Locate every blood parasite and identify its species.
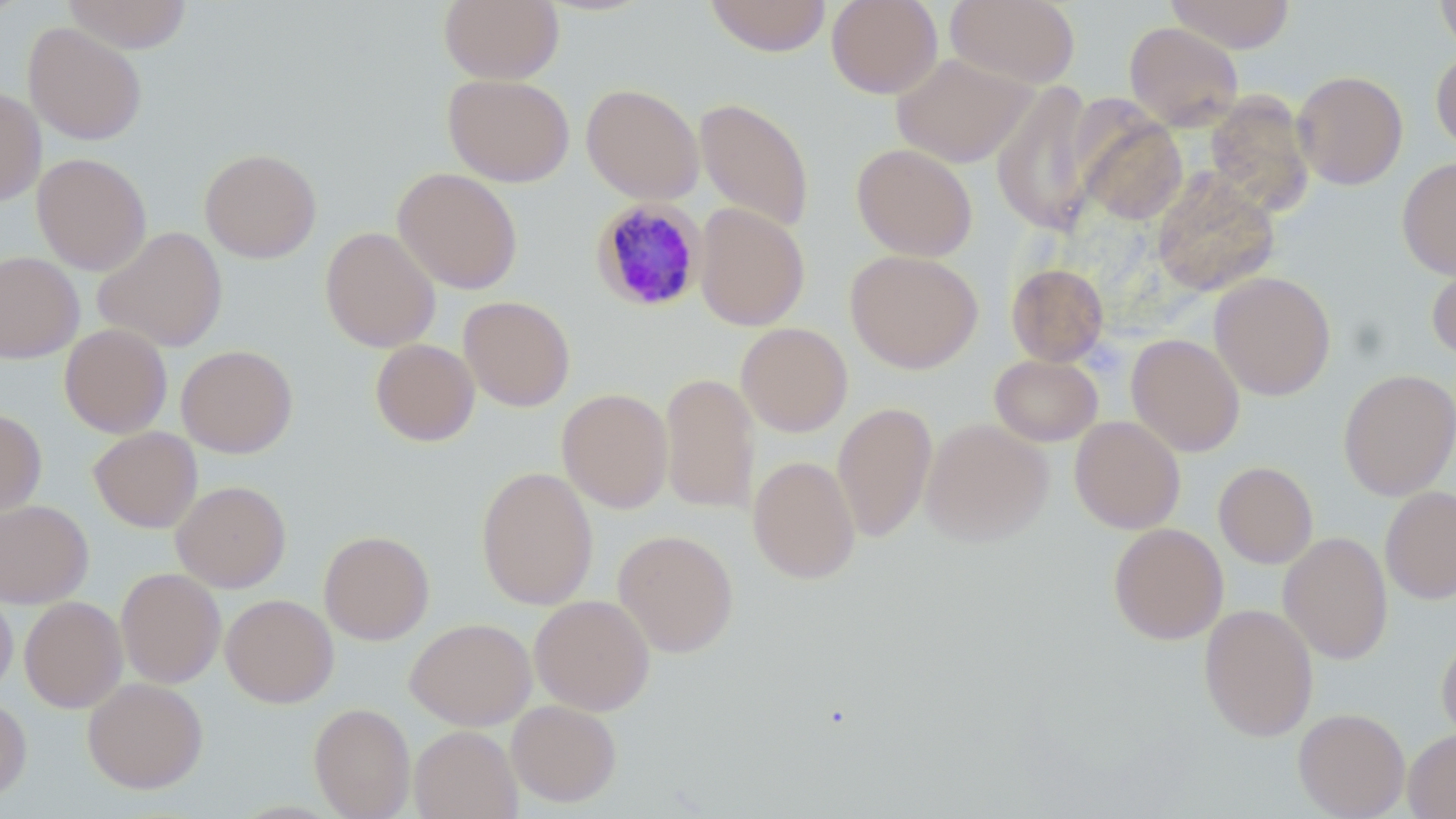
Approximate bounding boxes as (x1,y1)-(x2,y2) corner pairs in pixels.
Plasmodium malariae-infected red blood cells: (590,197)-(709,312).
No Plasmodium falciparum, Plasmodium ovale, Plasmodium vivax, Babesia divergens, or Trypanosoma brucei observed.

{
  "slide_level_diagnosis": "Plasmodium malariae",
  "uninfected_red_blood_cell_locations": "approximate bounding boxes as (x1,y1)-(x2,y2) corner pairs in pixels: (62,0)-(193,53), (438,0)-(564,84), (704,0)-(832,57), (826,0)-(943,98), (945,0)-(1081,89), (1164,0)-(1296,53), (1435,0)-(1456,56), (23,22)-(147,145), (1124,22)-(1243,131), (1431,49)-(1456,155), (891,52)-(1036,168), (1292,69)-(1408,189), (443,73)-(575,187), (991,82)-(1098,236), (581,83)-(704,204), (0,86)-(46,206), (1204,90)-(1315,217), (694,97)-(815,234), (1078,112)-(1187,226), (851,143)-(978,261), (199,147)-(321,263), (31,152)-(151,275), (1397,157)-(1456,280), (392,167)-(523,294), (1151,172)-(1280,296), (694,203)-(810,331), (320,226)-(440,352), (93,227)-(228,352), (845,249)-(983,373), (0,251)-(84,363), (1426,254)-(1456,361), (1006,262)-(1109,366), (1209,271)-(1336,400), (459,296)-(575,412), (736,322)-(852,437), (59,323)-(172,438), (1126,333)-(1245,457), (59,337)-(294,444), (370,339)-(480,446), (176,344)-(298,458), (989,354)-(1103,447), (1338,369)-(1456,500), (659,373)-(758,513), (556,388)-(673,513), (832,401)-(937,542), (0,408)-(47,517), (1069,415)-(1186,533), (920,417)-(1053,547), (88,426)-(202,532), (748,455)-(861,584), (1214,461)-(1318,568), (476,466)-(599,610), (171,480)-(291,592), (1380,485)-(1456,605), (0,499)-(93,608), (1108,523)-(1228,644), (613,529)-(739,657), (319,530)-(435,645), (1278,532)-(1393,664), (115,567)-(226,688), (0,584)-(18,698), (221,594)-(338,707), (529,595)-(655,715), (19,596)-(127,713), (1199,603)-(1319,741), (405,617)-(537,731), (1437,632)-(1456,743), (83,677)-(208,793), (0,694)-(32,800), (506,700)-(622,807), (309,702)-(416,819), (1293,708)-(1410,818), (409,725)-(522,819), (1404,728)-(1456,818)",
  "modality": "optical microscopy",
  "stain": "May-Grünwald-Giemsa",
  "magnification": "1000x",
  "image_size": "1456×819 pixels",
  "preparation": "thin blood smear",
  "field_of_view": "one of a larger specimen"
}